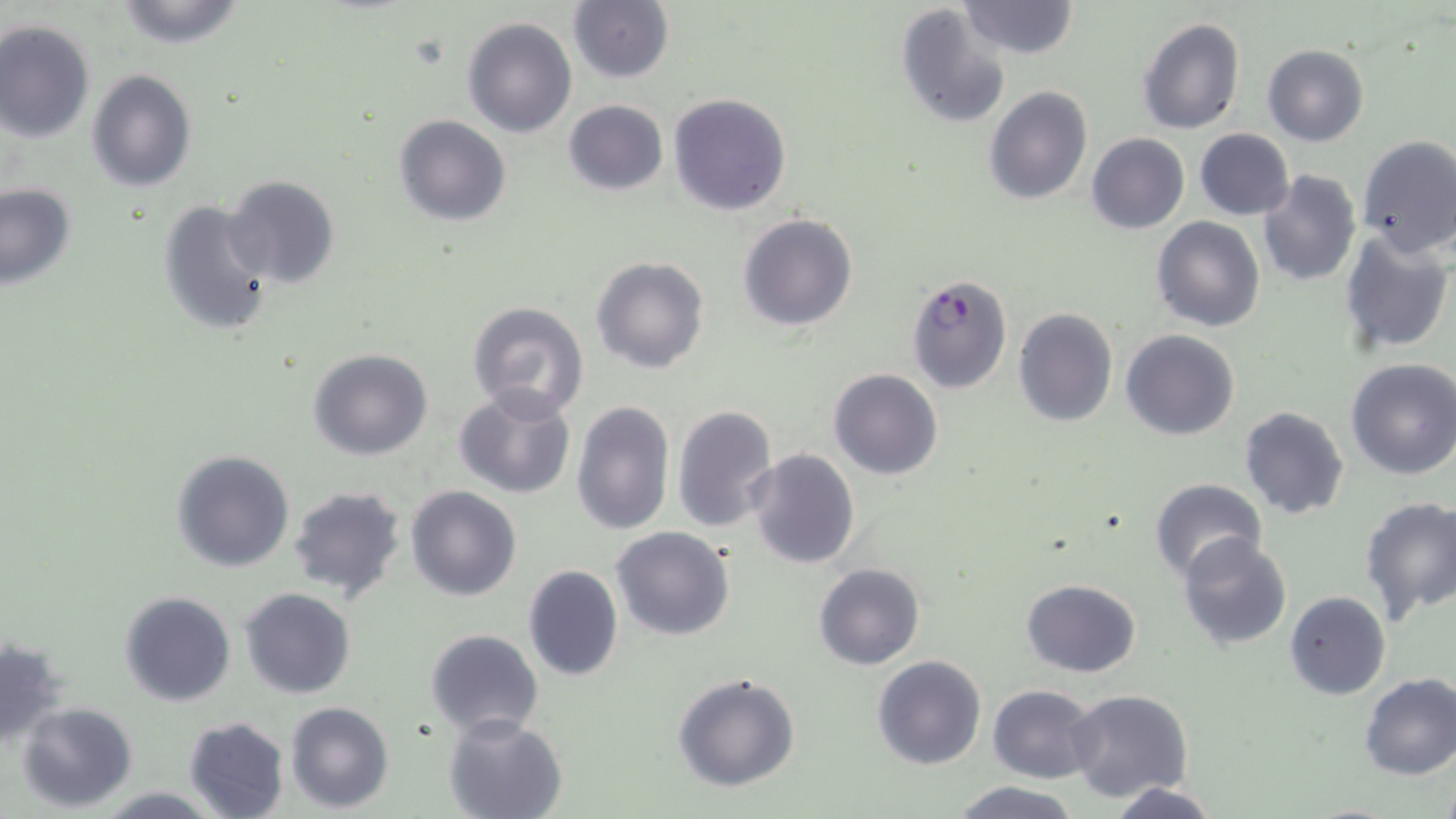

Summary:
  - Coordinate format: approximate bounding boxes as (x1, y1, x2, y2) in pixels
  - Plasmodium falciparum-infected red blood cell locations: (906, 271, 1012, 394)
  - Uninfected red blood cell locations: (112, 0, 247, 48), (569, 0, 675, 83), (958, 0, 1078, 60), (896, 3, 1012, 128), (1136, 16, 1246, 135), (463, 17, 577, 137), (0, 19, 95, 142), (1262, 44, 1369, 147), (86, 69, 196, 192), (983, 85, 1093, 205), (667, 92, 791, 216), (562, 100, 668, 196), (394, 115, 511, 226), (1194, 128, 1294, 220), (1086, 133, 1189, 233), (1356, 135, 1456, 258), (1257, 170, 1362, 287), (222, 176, 340, 289), (0, 182, 76, 290), (156, 198, 275, 337), (738, 212, 857, 332), (1150, 216, 1266, 332), (1339, 230, 1455, 355), (591, 256, 708, 373), (467, 301, 591, 420), (1013, 308, 1117, 427), (1121, 329, 1239, 441), (308, 347, 433, 459), (1345, 358, 1456, 479), (828, 368, 943, 480), (455, 387, 577, 498), (571, 401, 675, 537), (671, 403, 778, 533), (1239, 405, 1351, 521), (747, 448, 860, 569), (171, 449, 294, 572), (1148, 476, 1268, 581), (286, 485, 410, 603), (407, 485, 523, 601), (1359, 496, 1456, 622), (611, 527, 735, 641), (1176, 534, 1292, 650), (813, 563, 925, 670), (521, 566, 624, 682), (1021, 578, 1140, 677), (241, 588, 355, 698), (1285, 590, 1391, 700), (119, 591, 236, 707), (425, 629, 543, 736), (0, 636, 69, 751), (871, 656, 986, 770), (1358, 672, 1456, 780), (672, 673, 801, 791), (987, 685, 1097, 783), (1066, 689, 1194, 806), (18, 701, 138, 811), (285, 702, 394, 813), (445, 714, 566, 819), (183, 716, 291, 819), (949, 779, 1084, 818), (1109, 780, 1222, 818), (91, 787, 222, 818)
  - Slide-level diagnosis: Plasmodium falciparum
  - Modality: optical microscopy
  - Preparation: thin blood smear
  - Image size: 1456×819 pixels
  - Field of view: single
  - Magnification: 1000x
  - Stain: May-Grünwald-Giemsa